Name the parasite shown.
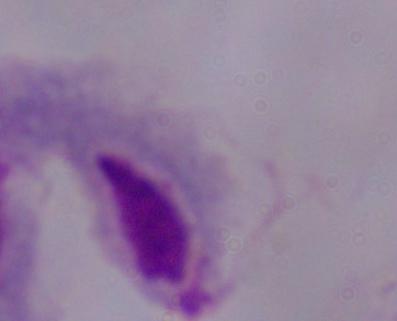

This is a trichomonad.

1000x magnification. Micrograph.